Assess this cell for malaria.
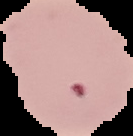
Parasitized.

Image is 133×136 pixels. From a thin blood film. Cell region segmented out of the field of view; the surrounding area is masked to black.